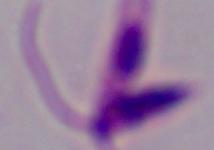

Summary:
  - Identification: Leishmania
  - Magnification: 1000x
  - Modality: micrograph